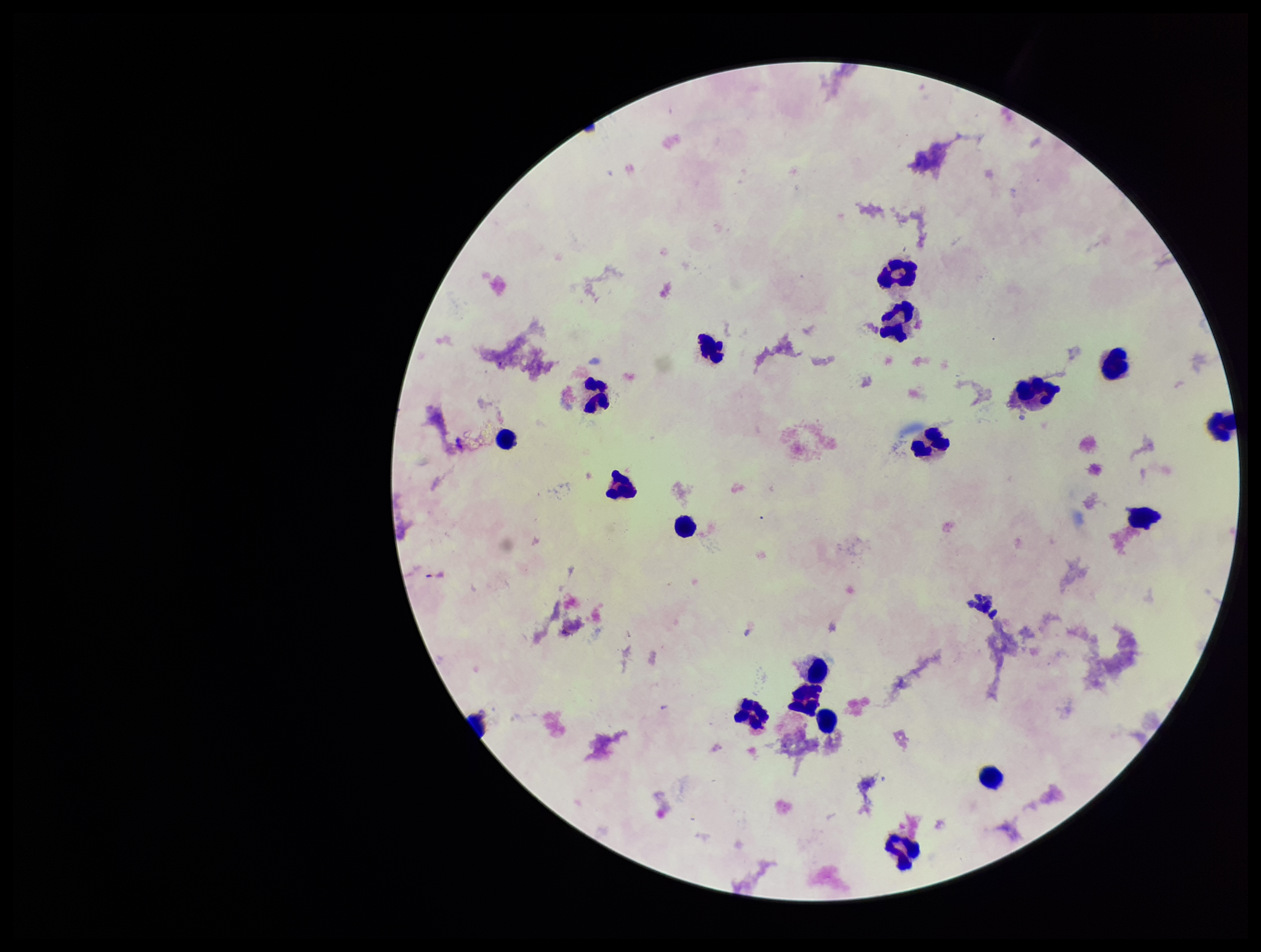

Summary:
  - Patient malaria status: negative
  - Stain: Giemsa
  - Preparation: thick smear
  - Field of view: one from this slide
  - Capture: smartphone photograph through the microscope eyepiece
  - Image size: 1261×952 pixels
  - Plasmodium parasites: none detected
  - Leukocyte count: 18
  - Parasite count: 0